Locate and identify every blood parasite.
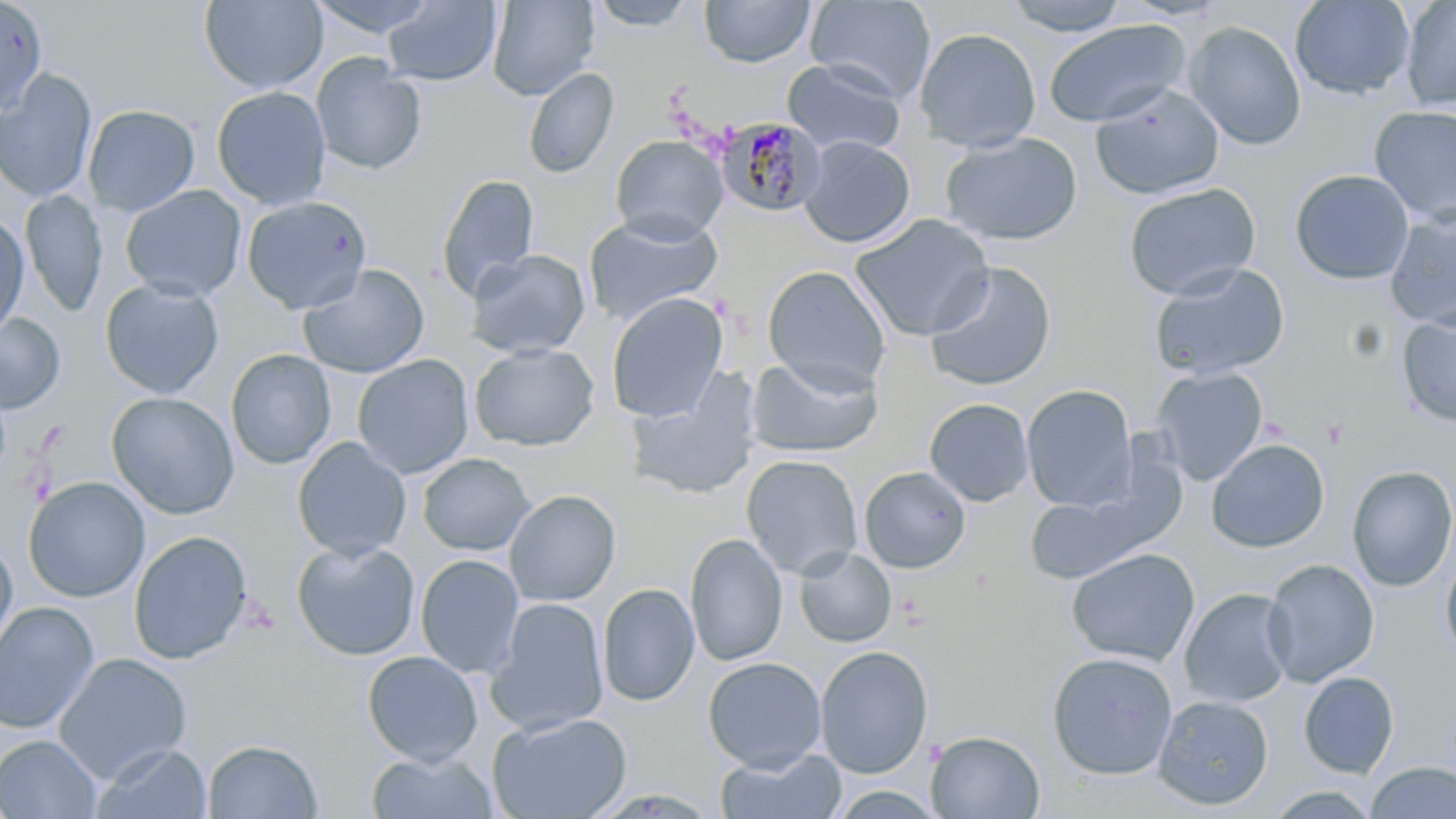
Approximate bounding boxes as (x1,y1)-(x2,y2) corner pairs in pixels.
Plasmodium malariae-infected red blood cells: (715,116)-(826,218).
No Plasmodium falciparum, Plasmodium ovale, Plasmodium vivax, Babesia divergens, or Trypanosoma brucei observed.

Summary:
  - Uninfected red blood cell locations: (199,0)-(327,94), (307,0)-(440,39), (487,0)-(599,101), (699,0)-(816,68), (804,0)-(937,103), (1000,0)-(1133,37), (1289,0)-(1416,100), (1400,0)-(1456,111), (0,1)-(48,115), (383,1)-(503,86), (587,1)-(698,31), (1043,20)-(1192,128), (1184,21)-(1307,149), (914,27)-(1042,152), (310,53)-(427,175), (782,59)-(907,157), (524,67)-(619,179), (0,69)-(98,203), (1089,84)-(1226,201), (211,86)-(331,210), (83,105)-(200,216), (1370,105)-(1456,225), (940,131)-(1083,246), (610,135)-(728,243), (799,135)-(915,248), (1289,169)-(1414,285), (437,174)-(539,300), (1123,183)-(1261,300), (120,185)-(246,302), (20,190)-(107,318), (241,196)-(372,315), (1385,208)-(1456,330), (0,212)-(29,341), (583,213)-(724,325), (851,213)-(995,341), (465,249)-(590,359), (924,261)-(1057,393), (1148,262)-(1290,381), (298,264)-(430,379), (762,265)-(890,393), (100,278)-(224,399), (606,292)-(729,423), (1396,309)-(1456,427), (0,313)-(65,414), (469,343)-(599,451), (225,349)-(336,469), (353,354)-(473,479), (745,355)-(882,458), (1150,367)-(1269,485), (627,370)-(762,501), (1022,384)-(1137,511), (106,391)-(239,520), (924,398)-(1034,506), (292,438)-(411,561), (1206,438)-(1330,554), (418,453)-(534,557), (741,454)-(863,579), (1024,463)-(1186,585), (1347,465)-(1456,591), (859,466)-(971,573), (23,476)-(150,602), (504,489)-(621,606), (128,530)-(253,665), (684,533)-(788,667), (0,536)-(17,665), (291,539)-(420,661), (793,547)-(896,649), (1065,548)-(1199,666), (1440,553)-(1456,666), (415,554)-(525,679), (1262,559)-(1380,686), (598,583)-(700,706), (1179,588)-(1296,708), (486,597)-(609,737), (0,602)-(100,735), (815,645)-(933,779), (362,650)-(483,764), (1046,651)-(1179,780), (53,652)-(192,784), (703,656)-(826,773), (1298,671)-(1399,778), (1152,694)-(1274,811), (487,712)-(631,818), (926,730)-(1045,818), (0,734)-(102,818), (203,739)-(323,818), (89,742)-(212,819), (715,748)-(847,819), (364,750)-(499,819), (1365,761)-(1456,819), (828,785)-(946,818), (1266,787)-(1381,818)
  - Slide-level diagnosis: Plasmodium malariae
  - Modality: light microscopy
  - Magnification: 1000x
  - Stain: May-Grünwald-Giemsa
  - Field of view: single
  - Image size: 1456×819 pixels
  - Preparation: thin blood smear